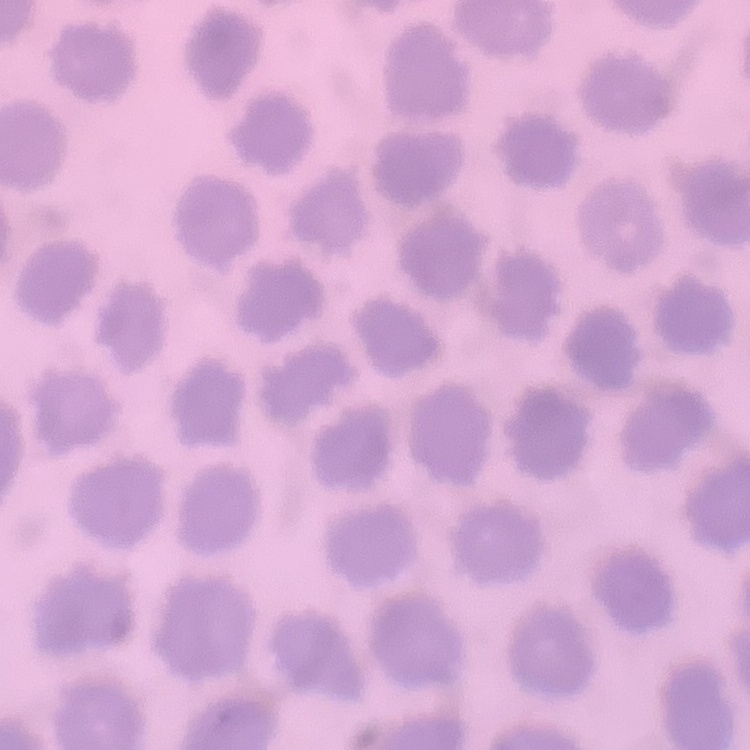
The red blood cells exhibit no rouleaux formation. Thin peripheral smear. Stained with either Field's or Giemsa. One tile cut from a larger photomicrograph.